Outline every leukocyte.
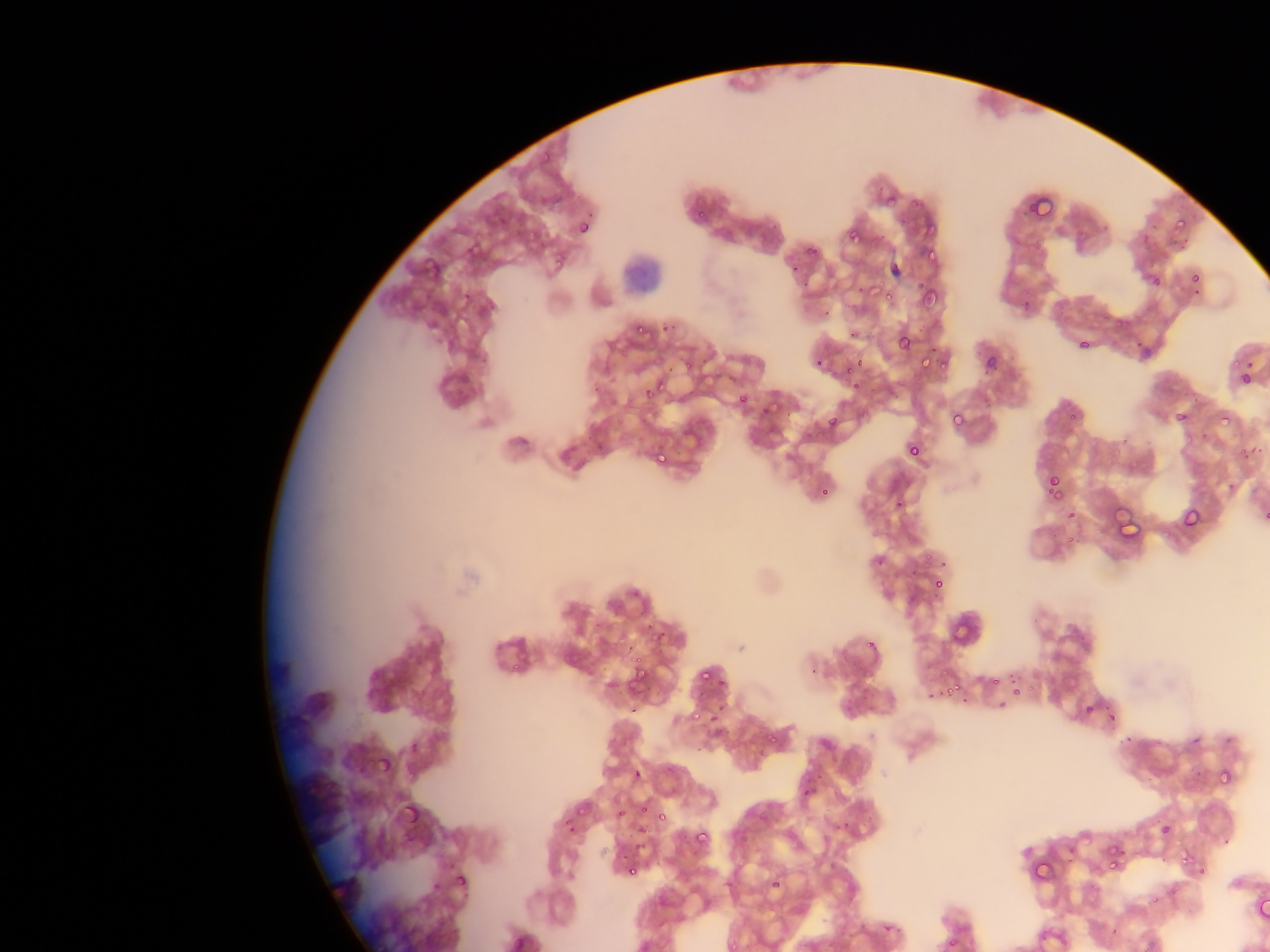

Approximate bounding boxes as {left, top, right, bottom} in pixels.
Leukocytes: {620, 245, 674, 289}.

Summary:
  - Plasmodium parasite locations: {886, 193, 897, 211}, {907, 194, 926, 209}, {1028, 197, 1054, 218}, {694, 210, 709, 225}, {1170, 213, 1194, 233}, {579, 214, 599, 231}, {497, 217, 504, 225}, {577, 218, 593, 236}, {921, 226, 937, 238}, {844, 228, 865, 244}, {803, 244, 820, 257}, {923, 250, 940, 267}, {550, 251, 567, 270}, {790, 257, 802, 271}, {1190, 271, 1202, 284}, {1147, 275, 1164, 289}, {799, 279, 811, 289}, {858, 281, 870, 295}, {916, 282, 941, 312}, {879, 286, 898, 302}, {462, 293, 473, 301}, {490, 297, 501, 307}, {817, 307, 840, 320}, {1113, 318, 1125, 331}, {633, 322, 645, 335}, {659, 323, 671, 333}, {845, 330, 865, 336}, {897, 332, 913, 350}, {1135, 338, 1149, 348}, {1078, 339, 1091, 351}, {1232, 350, 1244, 371}, {853, 352, 871, 369}, {916, 353, 930, 372}, {679, 355, 694, 369}, {935, 355, 954, 374}, {984, 355, 999, 372}, {815, 358, 825, 369}, {842, 368, 854, 376}, {1238, 370, 1252, 386}, {852, 372, 864, 396}, {653, 373, 676, 398}, {592, 384, 601, 394}, {644, 390, 651, 401}, {738, 393, 749, 405}, {759, 404, 773, 416}, {1175, 410, 1190, 425}, {1067, 412, 1079, 422}, {950, 414, 964, 431}, {1215, 414, 1231, 426}, {826, 416, 837, 429}, {1198, 431, 1209, 443}, {907, 443, 921, 456}, {1236, 443, 1253, 465}, {654, 447, 671, 466}, {1111, 449, 1123, 459}, {1046, 477, 1061, 493}, {1224, 481, 1239, 493}, {818, 486, 829, 497}, {1051, 490, 1068, 507}, {892, 503, 904, 513}, {1262, 503, 1270, 526}, {1182, 507, 1202, 529}, {1066, 509, 1076, 519}, {1065, 531, 1079, 545}, {920, 553, 937, 572}, {872, 555, 886, 567}, {941, 558, 948, 572}, {908, 566, 916, 577}, {931, 575, 946, 592}, {641, 623, 651, 633}, {653, 624, 669, 642}, {867, 635, 877, 646}, {624, 640, 636, 651}, {626, 657, 642, 667}, {804, 662, 821, 676}, {701, 668, 712, 685}, {1009, 670, 1020, 685}, {636, 671, 647, 681}, {988, 675, 1002, 689}, {719, 678, 725, 689}, {944, 681, 967, 694}, {1014, 688, 1022, 696}, {926, 690, 936, 699}, {843, 695, 875, 716}, {997, 699, 1007, 709}, {629, 702, 639, 716}, {1084, 703, 1096, 715}, {712, 706, 720, 725}, {688, 709, 702, 723}, {1107, 710, 1119, 724}, {762, 730, 779, 747}, {1124, 733, 1135, 744}, {1189, 734, 1207, 748}, {693, 744, 707, 760}, {409, 746, 423, 756}, {379, 747, 396, 773}, {666, 764, 678, 774}, {632, 768, 644, 781}, {1220, 772, 1232, 786}, {812, 774, 824, 784}, {799, 784, 818, 798}, {402, 792, 417, 819}, {639, 802, 651, 814}, {617, 808, 628, 818}, {655, 811, 666, 824}, {562, 817, 576, 832}, {832, 821, 852, 839}, {1160, 824, 1171, 835}, {694, 829, 710, 846}, {635, 841, 644, 851}, {1107, 845, 1127, 875}, {1180, 851, 1193, 864}, {1027, 861, 1055, 882}, {624, 863, 638, 878}, {1195, 867, 1210, 879}, {455, 873, 469, 889}, {770, 878, 781, 889}, {875, 923, 891, 933}
  - Field of view: single
  - Capture: mobile-phone photograph through a microscope
  - Image size: 1270×952 pixels
  - Country: Ghana
  - Preparation: thin blood smear